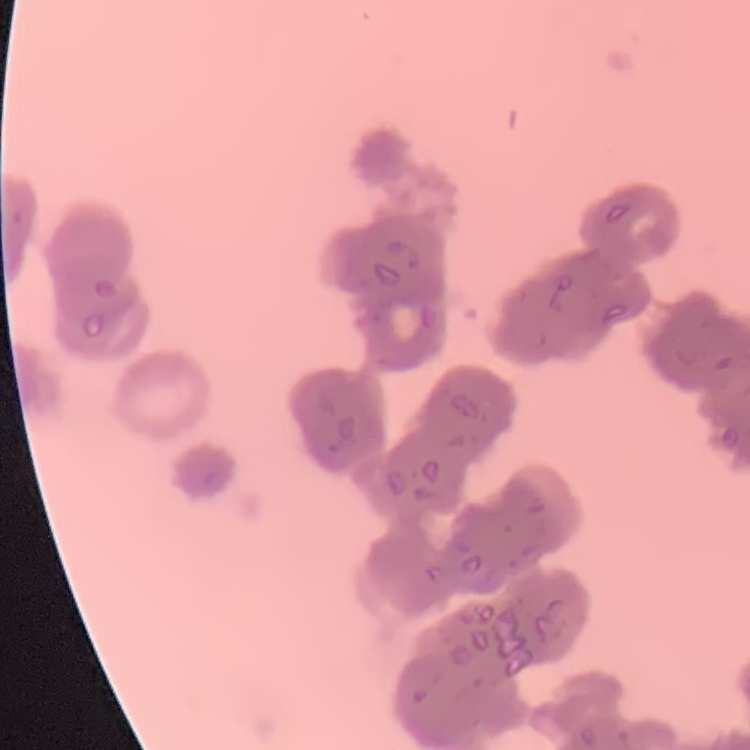
The red blood cells show rouleaux formation. Thin peripheral smear. One tile cut from a larger photomicrograph. Field's or Giemsa stain.